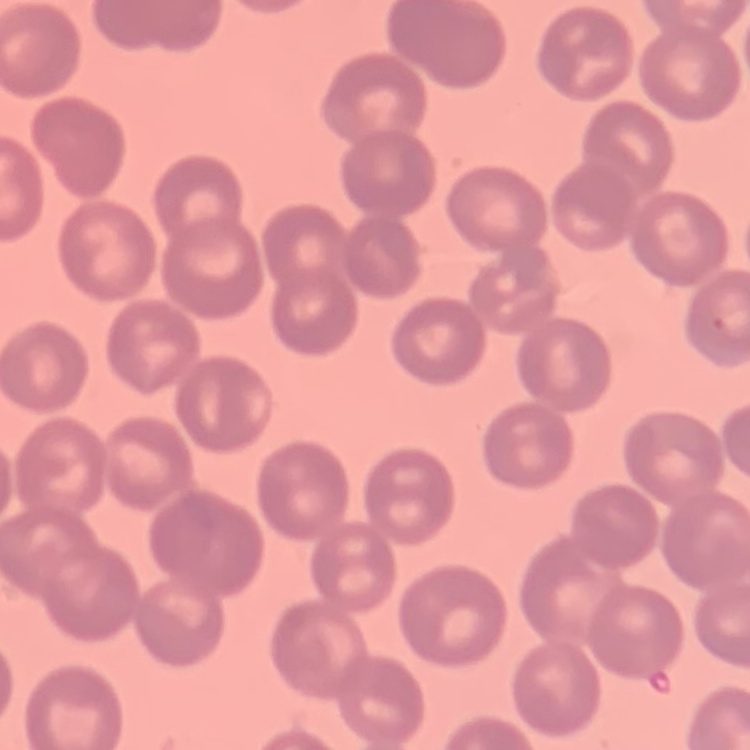

red_blood_cell_morphology: no rouleaux formation
stain: Field's or Giemsa
preparation: thin blood smear
image_type: one tile cut from a larger photomicrograph